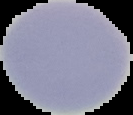

Summary:
  - Image type: segmented cell region with the area outside set to black
  - Preparation: thin blood film
  - Malaria status: uninfected
  - Image size: 133×115 pixels